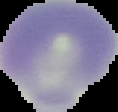

malaria status = uninfected
image size = 118×112 pixels
image type = segmented cell region with the area outside set to black
preparation = thin blood film